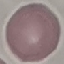
Result: no malaria parasites detected. Acquired by smartphone through the microscope eyepiece. Giemsa-stained preparation. Cell patch, automatically extracted from a larger field of view and resized to 64 × 64 pixels. Thin blood film.